Assess this cell for malaria.
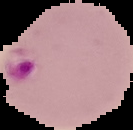

It is parasitized.

From a thin blood film. The area outside the segmented cell region is set to black. Image is 133×130 pixels.